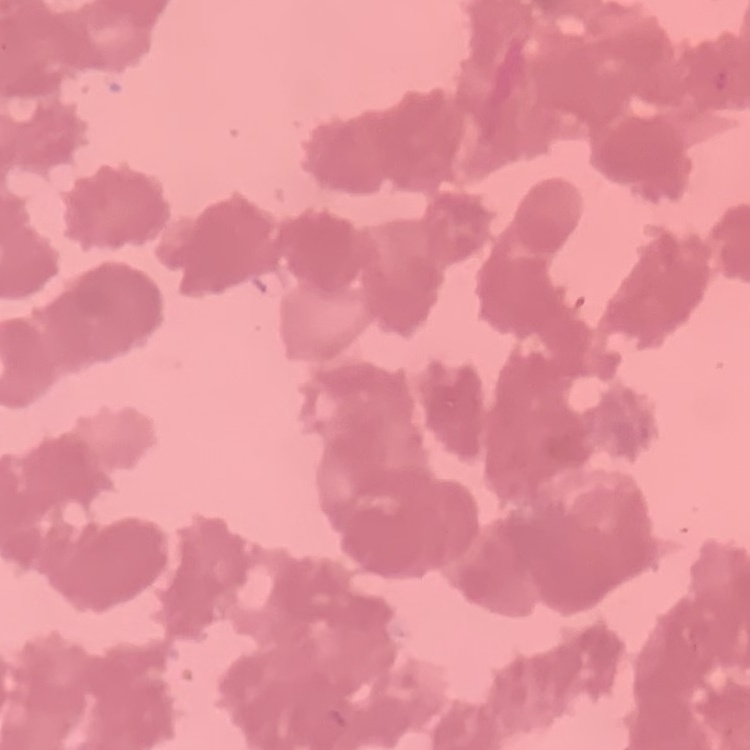

The erythrocytes show rouleaux formation. Thin blood smear. Square crop of a larger photomicrograph. Stained with either Field's or Giemsa.